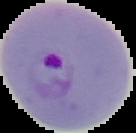

malaria status = parasitized
image size = 136×133 pixels
preparation = thin blood film
image type = segmented cell region with the area outside set to black